Assess this cell for malaria.
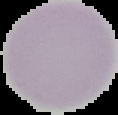
Uninfected.

{
  "image_size": "118×115 pixels",
  "preparation": "thin blood film",
  "image_type": "segmented cell region with the area outside set to black"
}